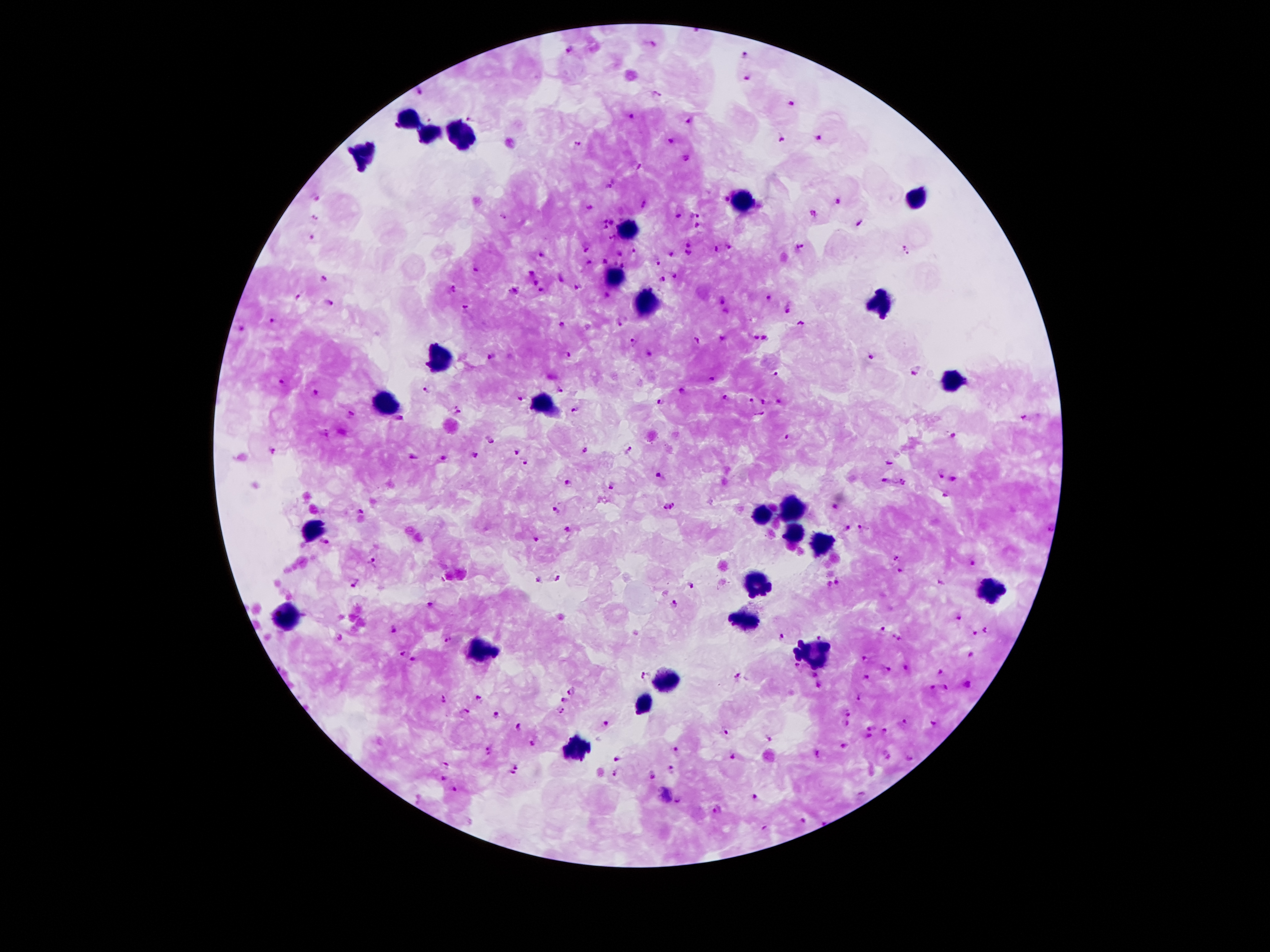
One field from this slide. Patient malaria status: infected with Plasmodium falciparum. Photographed through the microscope eyepiece with a smartphone camera. 100x magnification. Thick blood smear. Image is 1270×952 pixels. Giemsa stain.